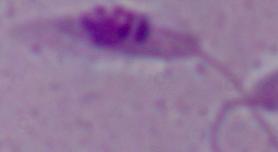
A Leishmania parasite is seen. 1000x magnification. Micrograph.